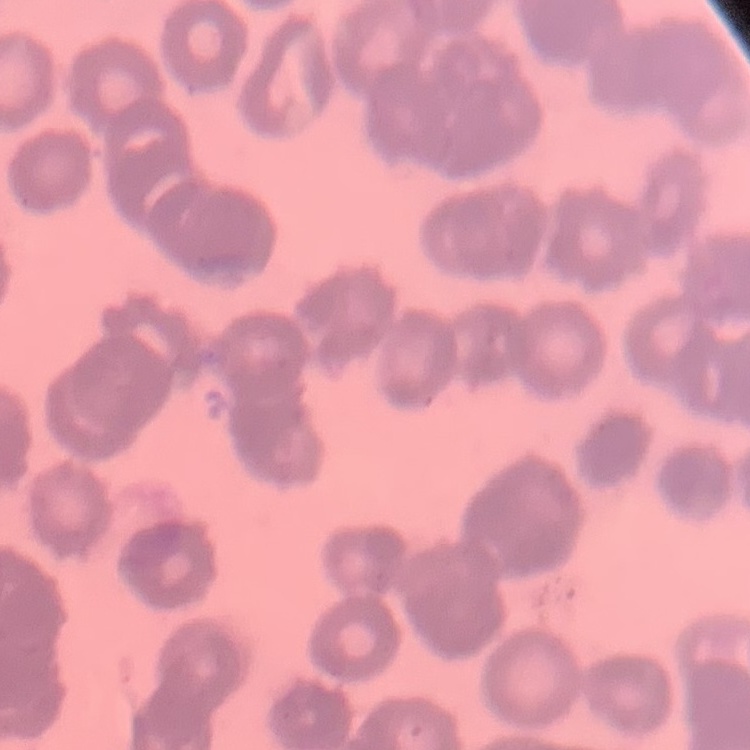 The erythrocytes exhibit rouleaux formation. Field's or Giemsa stain. One tile cut from a larger photomicrograph. Thin blood smear.